Report the malaria status of this cell.
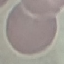

Uninfected.

Photographed with a smartphone camera at the microscope eyepiece. Automatically extracted cell patch, resized to 64 × 64 pixels. Thin blood film. Giemsa-stained preparation.